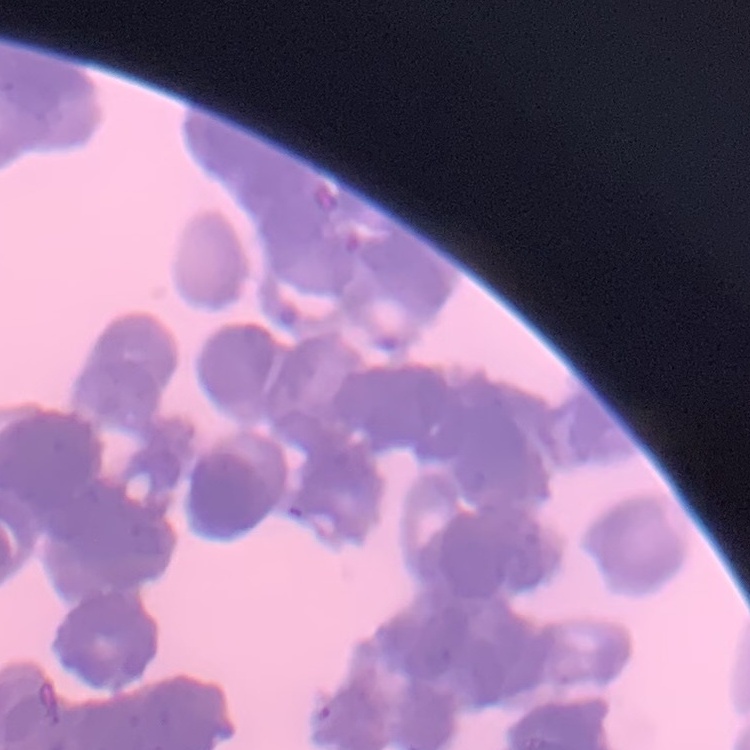
The erythrocytes show rouleaux formation. Thin blood film. Field's or Giemsa stain. One tile cut from a larger photomicrograph.